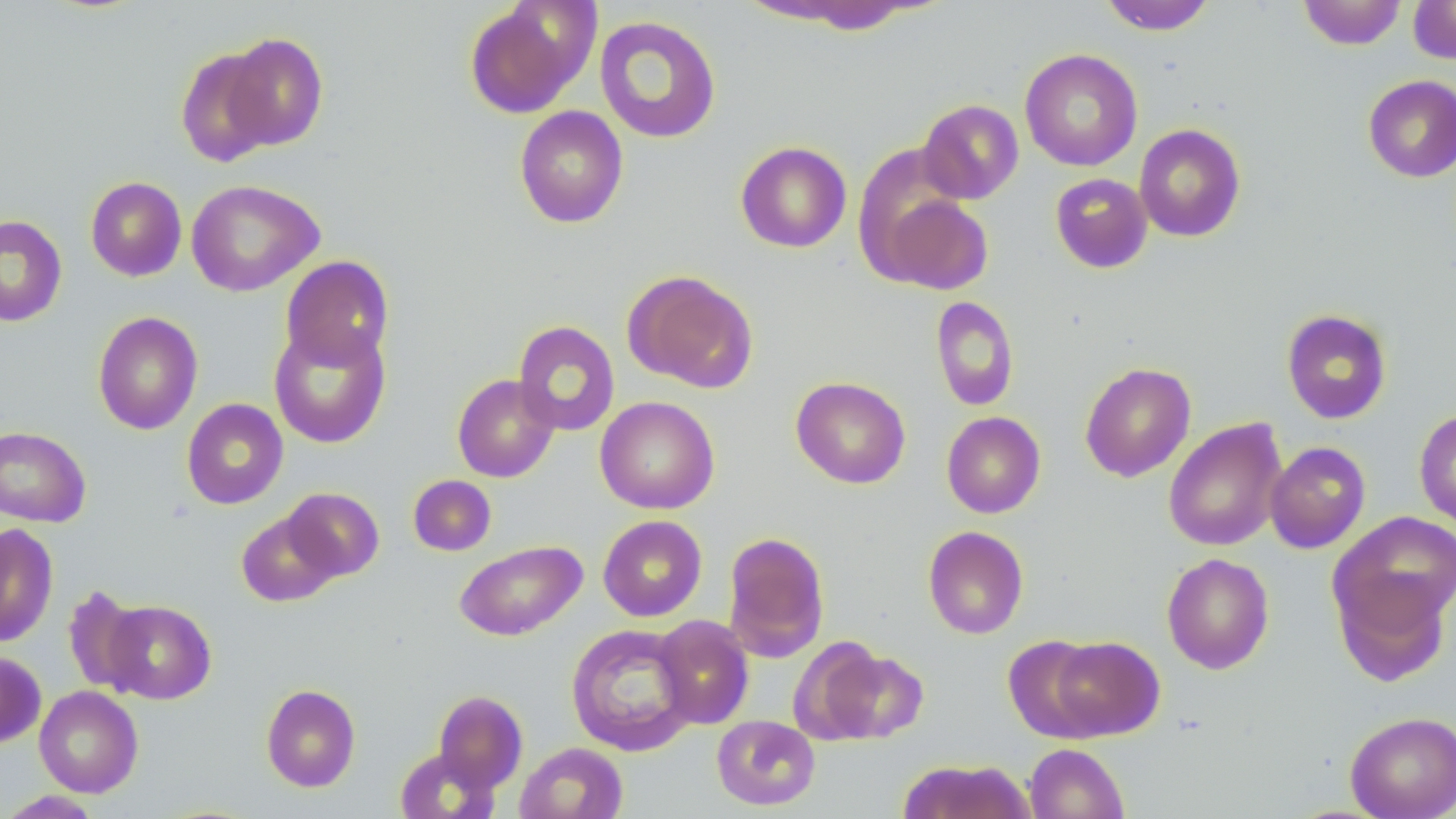

slide-level diagnosis = no evidence of blood parasites
magnification = 1000x
preparation = thin blood smear
image size = 1456×819 pixels
modality = light microscopy
stain = May-Grünwald-Giemsa
field of view = one of a larger specimen
uninfected red blood cell locations = approximate bounding boxes as (x1, y1, x2, y2) in pixels: (1099, 0, 1217, 35), (1298, 0, 1407, 50), (1408, 0, 1456, 65), (463, 1, 594, 119), (594, 15, 722, 144), (220, 33, 329, 151), (175, 47, 281, 167), (1020, 48, 1143, 171), (1362, 74, 1456, 182), (918, 99, 1024, 204), (514, 105, 629, 229), (1134, 123, 1246, 242), (735, 141, 851, 253), (1050, 173, 1153, 273), (85, 176, 187, 281), (185, 179, 324, 297), (874, 188, 993, 296), (0, 214, 67, 327), (280, 255, 395, 369), (623, 270, 758, 392), (930, 295, 1020, 412), (1281, 308, 1393, 424), (92, 311, 203, 435), (513, 320, 620, 436), (269, 321, 391, 449), (1079, 361, 1196, 482), (452, 374, 560, 482), (790, 376, 911, 489), (595, 395, 720, 514), (182, 398, 288, 509), (1414, 408, 1456, 531), (941, 411, 1046, 518), (1163, 418, 1287, 552), (0, 426, 91, 527), (1265, 441, 1370, 554), (408, 475, 496, 556), (282, 487, 384, 581), (237, 510, 341, 607), (1330, 512, 1456, 635), (598, 515, 707, 621), (0, 523, 59, 647), (923, 525, 1028, 639), (721, 532, 830, 662), (454, 540, 587, 641), (1161, 552, 1275, 674), (1333, 572, 1451, 686), (61, 586, 149, 693), (101, 599, 216, 704), (652, 615, 754, 729), (566, 623, 698, 756), (1003, 634, 1108, 742), (787, 636, 889, 746), (1048, 636, 1164, 740), (822, 645, 928, 744), (0, 651, 46, 748), (260, 683, 361, 792), (34, 685, 144, 797), (433, 689, 528, 794), (1345, 711, 1456, 819), (712, 714, 820, 810), (515, 742, 628, 819), (1024, 743, 1128, 819), (395, 747, 499, 819), (898, 759, 1035, 818), (1, 790, 105, 818)